Assess the morphology of the red blood cells.
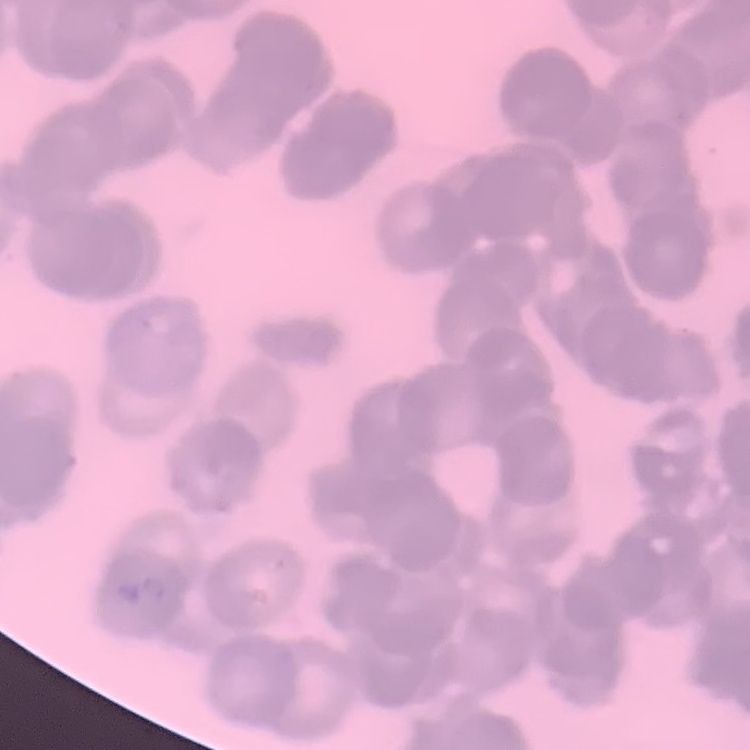

Rouleaux formation.

Summary:
  - Image type: square crop of a larger photomicrograph
  - Preparation: thin peripheral smear
  - Stain: Field's or Giemsa